Point out every malaria parasite and every leukocyte.
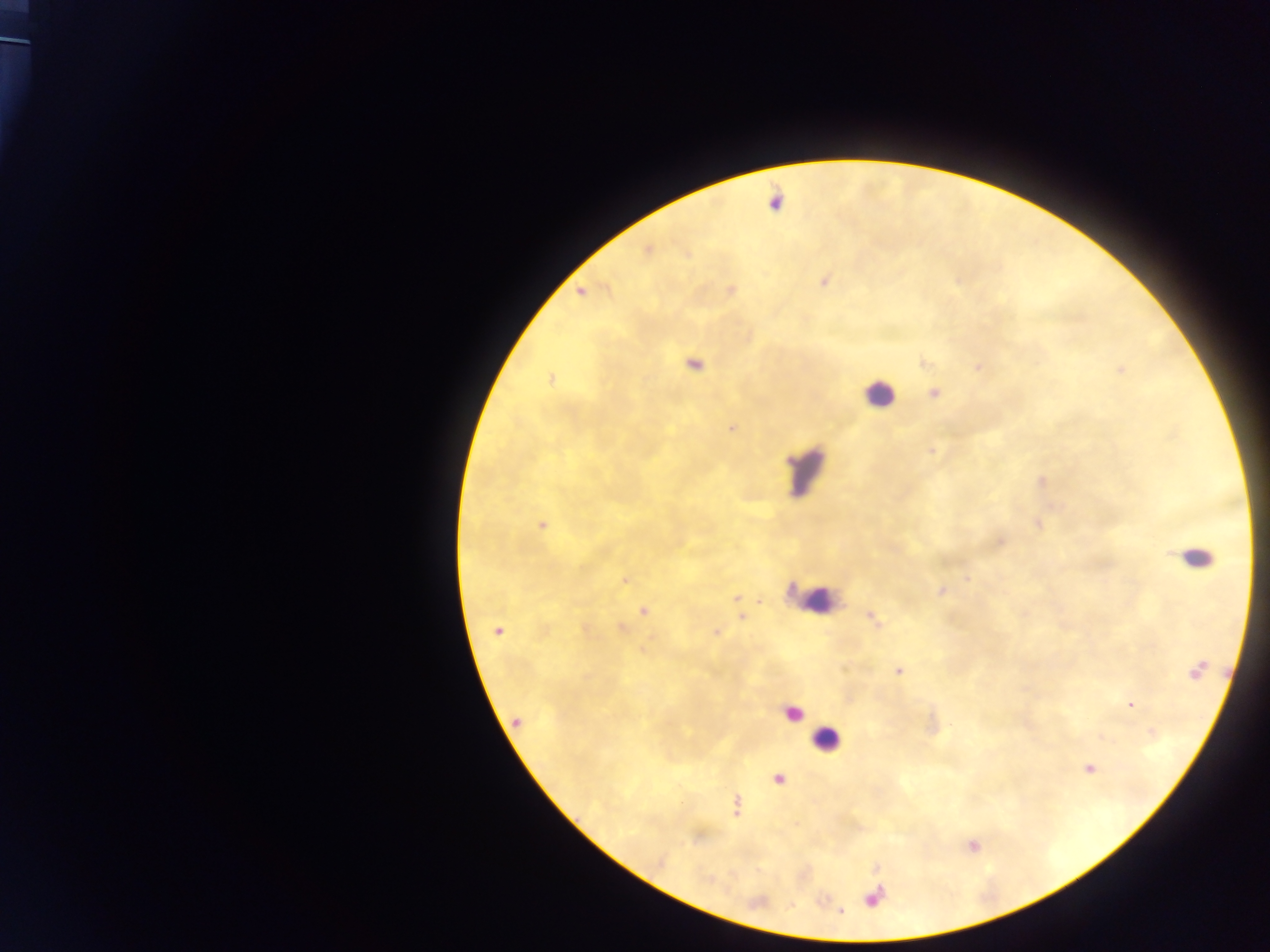

Approximate centers as {x, y} in pixels.
Malaria parasites: {775, 202}, {647, 251}, {686, 255}, {824, 282}, {732, 290}, {979, 366}, {1121, 369}, {550, 380}, {933, 392}, {732, 429}, {931, 451}, {542, 524}, {1000, 542}, {967, 579}, {625, 580}, {941, 591}, {644, 610}, {872, 618}, {622, 627}, {497, 631}, {717, 633}, {899, 671}, {1129, 705}, {517, 721}, {1089, 768}, {779, 779}, {736, 806}.
Leukocytes: {878, 394}, {806, 471}, {1195, 557}, {816, 590}, {793, 715}, {827, 740}.
One object is labeled both malaria parasite and leukocyte by the source: {695, 365}.

Photographed through a microscope with a mobile-phone camera. One field of view. Thick blood smear. Collected in Ghana. Image is 1270×952 pixels.